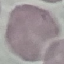

Summary:
  - Malaria status: uninfected
  - Preparation: thin blood film
  - Stain: Giemsa
  - Image type: automatically extracted cell patch, resized to 64 × 64 pixels
  - Capture: smartphone camera at the microscope eyepiece